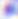

{
  "identification": "Toxoplasma gondii",
  "magnification": "400x",
  "modality": "photomicrograph"
}